State which parasite is depicted.
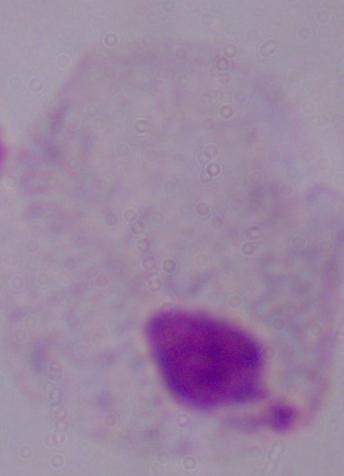

A trichomonad.

Summary:
  - Magnification: 1000x
  - Modality: micrograph